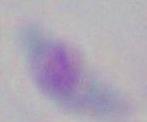
identification = Toxoplasma gondii
magnification = 1000x
modality = micrograph